Name the parasite shown.
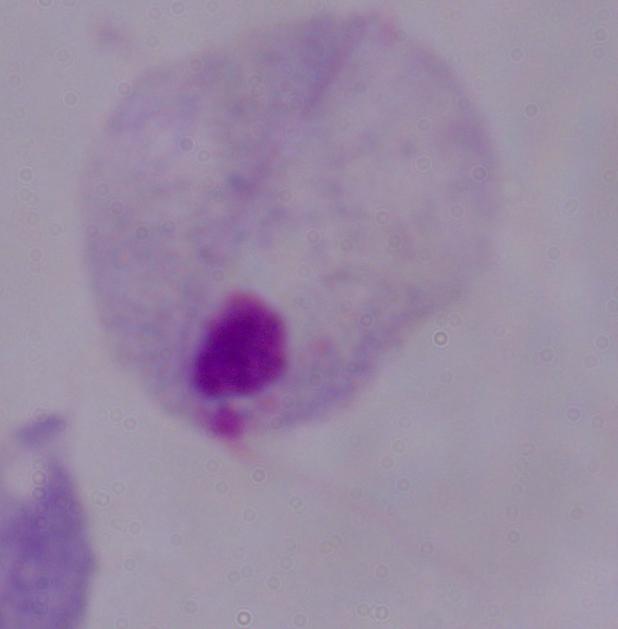

A trichomonad.

1000x magnification. Photomicrograph.